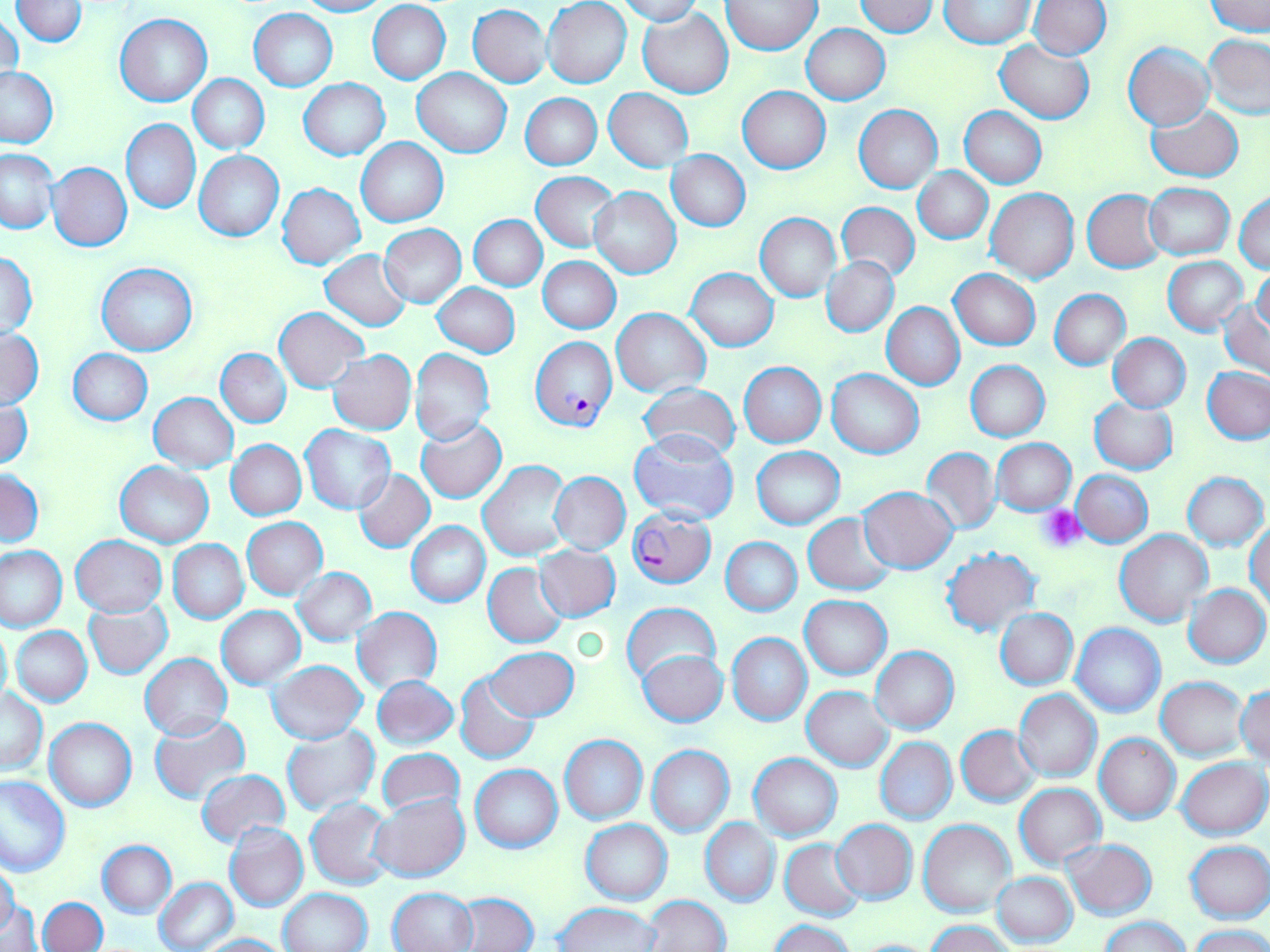
Approximate bounding boxes as named x1/y1/x2/y2 corners in pixels. Uninfected red blood cell locations: (x1=12, y1=0, x2=89, y2=46), (x1=295, y1=0, x2=389, y2=16), (x1=543, y1=0, x2=632, y2=89), (x1=616, y1=0, x2=702, y2=25), (x1=723, y1=1, x2=821, y2=54), (x1=853, y1=1, x2=938, y2=36), (x1=940, y1=1, x2=1033, y2=47), (x1=1027, y1=1, x2=1111, y2=59), (x1=1205, y1=1, x2=1269, y2=34), (x1=367, y1=2, x2=451, y2=84), (x1=468, y1=5, x2=552, y2=87), (x1=638, y1=7, x2=734, y2=97), (x1=249, y1=9, x2=337, y2=91), (x1=1, y1=11, x2=24, y2=86), (x1=115, y1=14, x2=211, y2=106), (x1=801, y1=24, x2=890, y2=103), (x1=1203, y1=35, x2=1270, y2=119), (x1=994, y1=40, x2=1095, y2=124), (x1=1123, y1=43, x2=1214, y2=131), (x1=0, y1=67, x2=57, y2=147), (x1=413, y1=67, x2=512, y2=157), (x1=189, y1=74, x2=269, y2=153), (x1=298, y1=79, x2=390, y2=160), (x1=738, y1=86, x2=831, y2=173), (x1=605, y1=88, x2=693, y2=172), (x1=520, y1=93, x2=602, y2=169), (x1=1146, y1=103, x2=1244, y2=183), (x1=855, y1=105, x2=942, y2=192), (x1=961, y1=107, x2=1046, y2=188), (x1=121, y1=118, x2=200, y2=213), (x1=356, y1=138, x2=448, y2=227), (x1=0, y1=149, x2=57, y2=232), (x1=194, y1=150, x2=285, y2=241), (x1=666, y1=150, x2=750, y2=230), (x1=48, y1=162, x2=132, y2=252), (x1=913, y1=168, x2=992, y2=243), (x1=533, y1=171, x2=620, y2=252), (x1=277, y1=183, x2=365, y2=269), (x1=1145, y1=183, x2=1235, y2=259), (x1=591, y1=188, x2=681, y2=278), (x1=986, y1=188, x2=1079, y2=282), (x1=1082, y1=189, x2=1166, y2=273), (x1=1234, y1=190, x2=1270, y2=275), (x1=836, y1=201, x2=919, y2=282), (x1=756, y1=213, x2=841, y2=302), (x1=471, y1=215, x2=547, y2=291), (x1=379, y1=224, x2=466, y2=307), (x1=321, y1=249, x2=412, y2=330), (x1=1, y1=251, x2=38, y2=336), (x1=538, y1=256, x2=621, y2=333), (x1=822, y1=256, x2=898, y2=336), (x1=1163, y1=256, x2=1248, y2=336), (x1=97, y1=264, x2=197, y2=355), (x1=1252, y1=264, x2=1270, y2=337), (x1=687, y1=268, x2=778, y2=351), (x1=950, y1=270, x2=1039, y2=349), (x1=434, y1=284, x2=520, y2=357), (x1=1049, y1=289, x2=1130, y2=369), (x1=1219, y1=299, x2=1270, y2=379), (x1=882, y1=302, x2=965, y2=389), (x1=274, y1=307, x2=367, y2=391), (x1=612, y1=308, x2=710, y2=396), (x1=0, y1=329, x2=43, y2=410), (x1=1109, y1=334, x2=1191, y2=412), (x1=67, y1=348, x2=153, y2=425), (x1=216, y1=349, x2=291, y2=427), (x1=410, y1=349, x2=494, y2=446), (x1=327, y1=350, x2=416, y2=434), (x1=965, y1=360, x2=1049, y2=442), (x1=740, y1=362, x2=825, y2=447), (x1=1202, y1=367, x2=1270, y2=443), (x1=827, y1=369, x2=923, y2=458), (x1=637, y1=383, x2=742, y2=463), (x1=149, y1=393, x2=237, y2=473), (x1=0, y1=398, x2=33, y2=470), (x1=1089, y1=398, x2=1177, y2=473), (x1=416, y1=418, x2=508, y2=503), (x1=300, y1=425, x2=395, y2=514), (x1=629, y1=431, x2=739, y2=525), (x1=992, y1=438, x2=1076, y2=514), (x1=226, y1=440, x2=306, y2=520), (x1=752, y1=446, x2=845, y2=529), (x1=921, y1=448, x2=1000, y2=535), (x1=115, y1=461, x2=212, y2=547), (x1=479, y1=461, x2=572, y2=560), (x1=0, y1=469, x2=44, y2=547), (x1=353, y1=469, x2=434, y2=552), (x1=1073, y1=470, x2=1153, y2=546), (x1=551, y1=472, x2=630, y2=555), (x1=1182, y1=472, x2=1268, y2=551), (x1=859, y1=487, x2=958, y2=573), (x1=803, y1=513, x2=898, y2=595), (x1=242, y1=518, x2=327, y2=599), (x1=1246, y1=520, x2=1269, y2=610), (x1=407, y1=521, x2=490, y2=607), (x1=1116, y1=530, x2=1213, y2=626), (x1=71, y1=535, x2=167, y2=616), (x1=720, y1=537, x2=801, y2=616), (x1=169, y1=540, x2=248, y2=623), (x1=0, y1=545, x2=67, y2=632), (x1=534, y1=545, x2=620, y2=621), (x1=941, y1=546, x2=1041, y2=635), (x1=483, y1=562, x2=567, y2=647), (x1=293, y1=567, x2=376, y2=645), (x1=1185, y1=584, x2=1269, y2=667), (x1=800, y1=596, x2=891, y2=679), (x1=85, y1=601, x2=173, y2=679), (x1=621, y1=601, x2=721, y2=688), (x1=216, y1=606, x2=304, y2=689), (x1=352, y1=607, x2=442, y2=693), (x1=995, y1=608, x2=1078, y2=689), (x1=1072, y1=624, x2=1165, y2=718), (x1=0, y1=625, x2=11, y2=708), (x1=13, y1=626, x2=92, y2=705), (x1=727, y1=633, x2=811, y2=725), (x1=484, y1=645, x2=579, y2=722), (x1=870, y1=646, x2=959, y2=734), (x1=637, y1=650, x2=728, y2=726), (x1=141, y1=654, x2=233, y2=740), (x1=267, y1=660, x2=368, y2=745), (x1=454, y1=672, x2=541, y2=763), (x1=372, y1=675, x2=458, y2=750), (x1=1157, y1=677, x2=1250, y2=760), (x1=1236, y1=685, x2=1270, y2=764), (x1=801, y1=686, x2=893, y2=770), (x1=1, y1=689, x2=47, y2=775), (x1=1013, y1=689, x2=1101, y2=782), (x1=150, y1=716, x2=250, y2=803), (x1=45, y1=718, x2=137, y2=812), (x1=281, y1=725, x2=379, y2=815), (x1=956, y1=725, x2=1039, y2=806), (x1=1094, y1=733, x2=1181, y2=824), (x1=560, y1=735, x2=648, y2=824), (x1=875, y1=738, x2=957, y2=824), (x1=646, y1=744, x2=734, y2=837), (x1=376, y1=747, x2=465, y2=820), (x1=749, y1=753, x2=842, y2=840), (x1=1177, y1=758, x2=1268, y2=839), (x1=470, y1=764, x2=562, y2=852), (x1=195, y1=769, x2=289, y2=848), (x1=0, y1=775, x2=69, y2=876), (x1=1015, y1=784, x2=1105, y2=867), (x1=370, y1=793, x2=470, y2=881), (x1=306, y1=799, x2=395, y2=889), (x1=700, y1=819, x2=780, y2=906), (x1=918, y1=819, x2=1015, y2=919), (x1=581, y1=820, x2=672, y2=904), (x1=830, y1=820, x2=917, y2=903), (x1=224, y1=823, x2=307, y2=912), (x1=780, y1=839, x2=867, y2=921), (x1=1061, y1=839, x2=1156, y2=919), (x1=98, y1=840, x2=176, y2=917), (x1=1184, y1=840, x2=1269, y2=923), (x1=0, y1=864, x2=19, y2=937), (x1=993, y1=872, x2=1077, y2=948), (x1=155, y1=878, x2=236, y2=951), (x1=278, y1=888, x2=373, y2=952), (x1=390, y1=888, x2=477, y2=952), (x1=453, y1=892, x2=538, y2=952), (x1=643, y1=895, x2=730, y2=952), (x1=38, y1=897, x2=107, y2=951), (x1=4, y1=900, x2=40, y2=952), (x1=554, y1=902, x2=662, y2=951), (x1=1101, y1=915, x2=1190, y2=952), (x1=770, y1=919, x2=856, y2=952), (x1=927, y1=921, x2=1013, y2=952), (x1=1189, y1=925, x2=1270, y2=952), (x1=201, y1=933, x2=290, y2=952), (x1=845, y1=937, x2=938, y2=952). Plasmodium falciparum-infected red blood cell locations: (x1=530, y1=337, x2=617, y2=429), (x1=628, y1=508, x2=715, y2=587). Platelet locations: (x1=1039, y1=505, x2=1086, y2=552). Slide-level diagnosis: Plasmodium falciparum. Image is 1270×952 pixels. May-Grünwald-Giemsa-stained preparation. Light microscopy. Single field of view. Captured at 1000x magnification. Thin blood film.